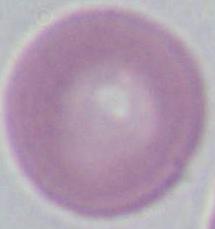
1000x magnification. Micrograph. An erythrocyte is seen.